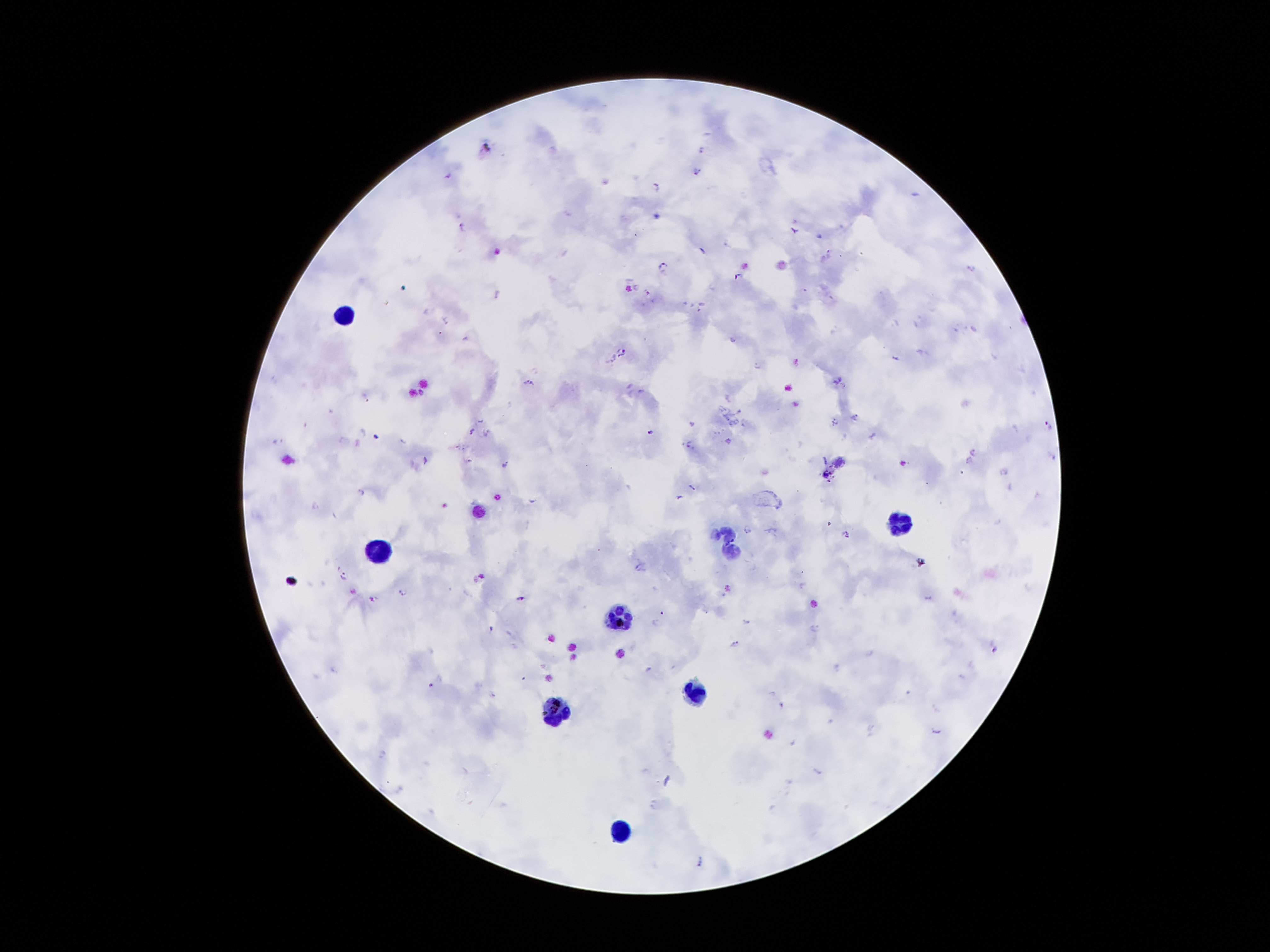
{
  "field_of_view": "single",
  "leukocyte_locations": "approximate centers as {x, y} in pixels: {344, 315}, {895, 520}, {726, 529}, {730, 555}, {379, 556}, {622, 615}, {697, 691}, {557, 713}",
  "image_size": "1270×952 pixels",
  "patient_malaria_status": "positive for Plasmodium falciparum",
  "magnification": "100x",
  "capture": "smartphone camera through the microscope eyepiece",
  "stain": "Giemsa",
  "plasmodium_parasite_locations": "approximate centers as {x, y} in pixels: {484, 146}, {699, 149}, {695, 170}, {657, 186}, {461, 224}, {793, 229}, {663, 264}, {971, 268}, {736, 276}, {634, 285}, {647, 292}, {497, 293}, {444, 320}, {466, 339}, {732, 339}, {620, 350}, {894, 358}, {796, 361}, {756, 365}, {836, 379}, {529, 381}, {641, 391}, {854, 417}, {692, 422}, {835, 422}, {1048, 424}, {471, 430}, {486, 431}, {650, 432}, {376, 436}, {689, 442}, {974, 453}, {1053, 458}, {425, 459}, {967, 462}, {504, 465}, {1005, 473}, {691, 487}, {360, 492}, {678, 497}, {531, 500}, {749, 531}, {846, 532}, {920, 561}, {342, 576}, {481, 578}, {403, 591}, {520, 598}, {927, 598}, {748, 623}, {812, 626}, {489, 628}, {734, 644}, {996, 649}, {429, 684}, {935, 731}, {381, 752}, {819, 771}, {699, 859}",
  "preparation": "thick blood smear"
}